Identify the parasite.
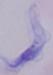
This is a trypanosome.

Micrograph. 1000x magnification.